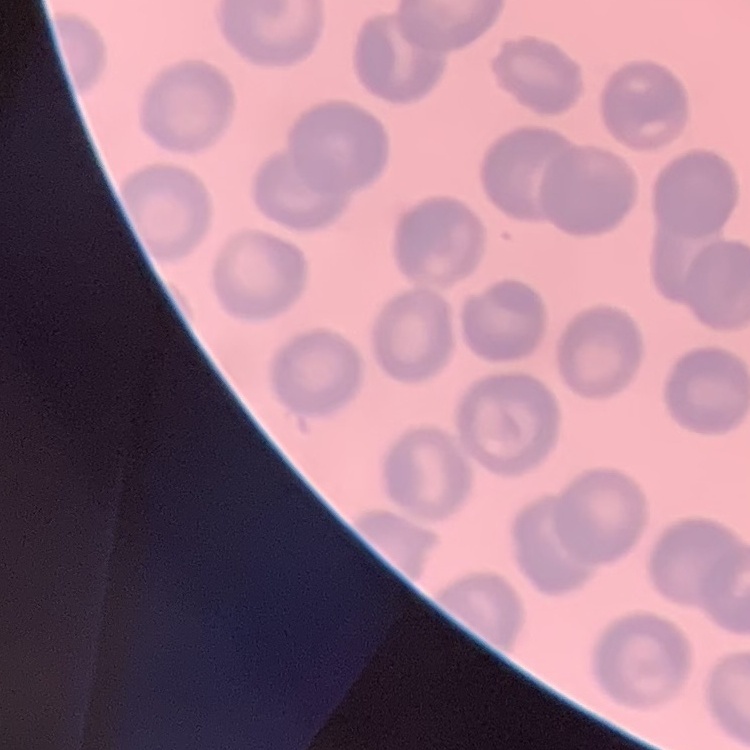

The erythrocytes show no rouleaux formation. Field's or Giemsa stain. Thin peripheral smear. Square crop of a larger photomicrograph.